Assess for Plasmodium parasites.
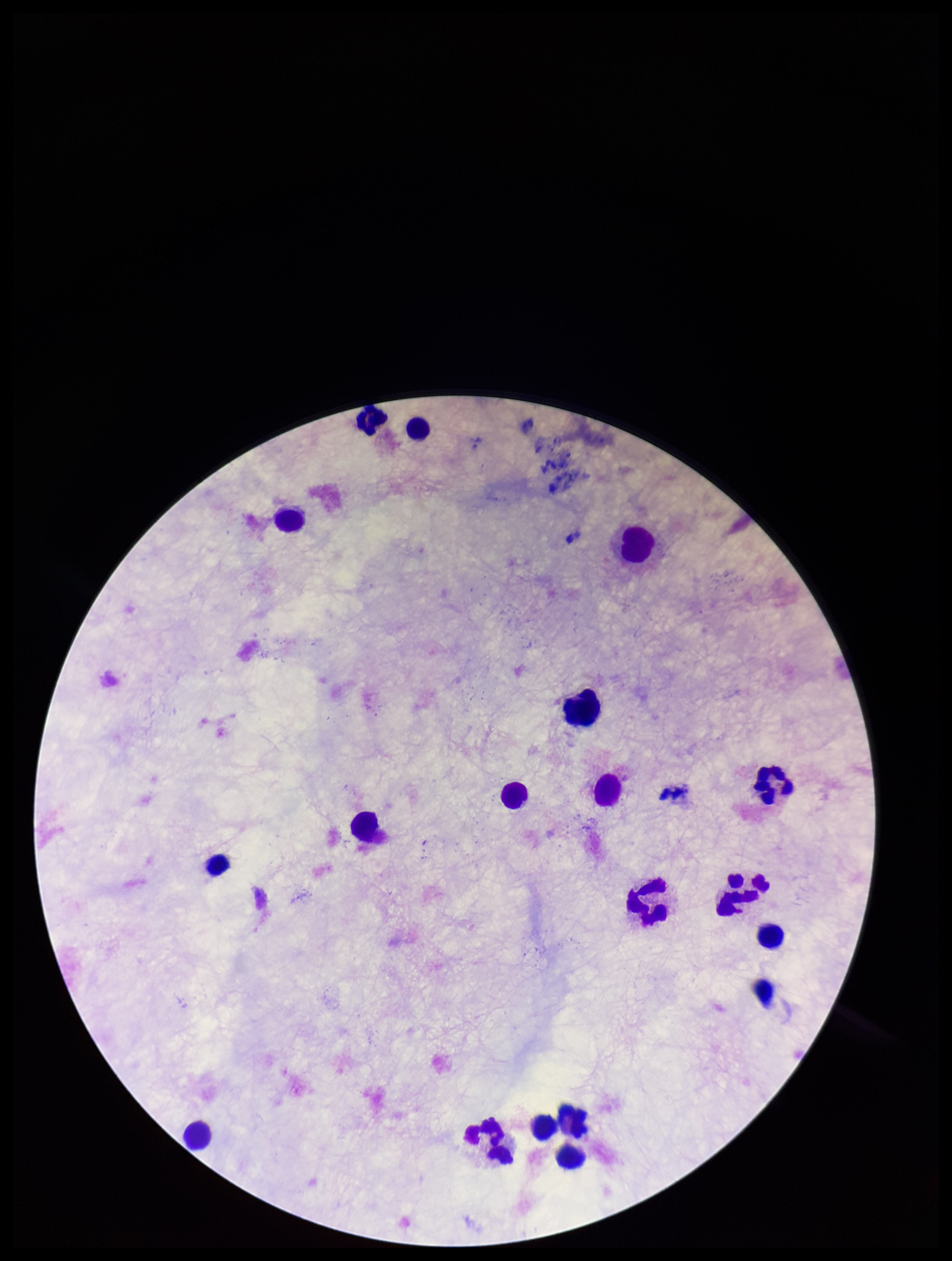

None identified.

Summary:
  - Field of view: one from this slide
  - Capture: smartphone photograph through the microscope eyepiece
  - Leukocyte count: 17
  - Preparation: thick blood smear
  - Patient malaria status: negative
  - Image size: 952×1261 pixels
  - Parasite count: 0
  - Stain: Giemsa